Report the malaria status of this cell.
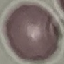

It is uninfected.

Summary:
  - Capture: smartphone through the microscope eyepiece
  - Preparation: thin smear
  - Stain: Giemsa
  - Image type: automatically extracted cell patch, resized to 64 × 64 pixels